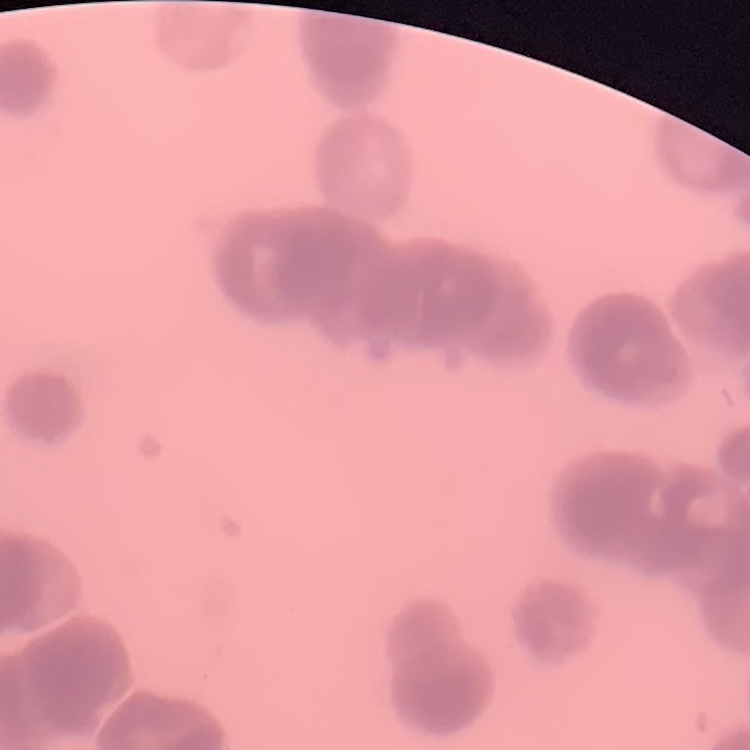
red blood cell morphology = rouleaux formation
preparation = thin blood film
image type = one tile cut from a larger photomicrograph
stain = Field's or Giemsa